State the blood parasite species.
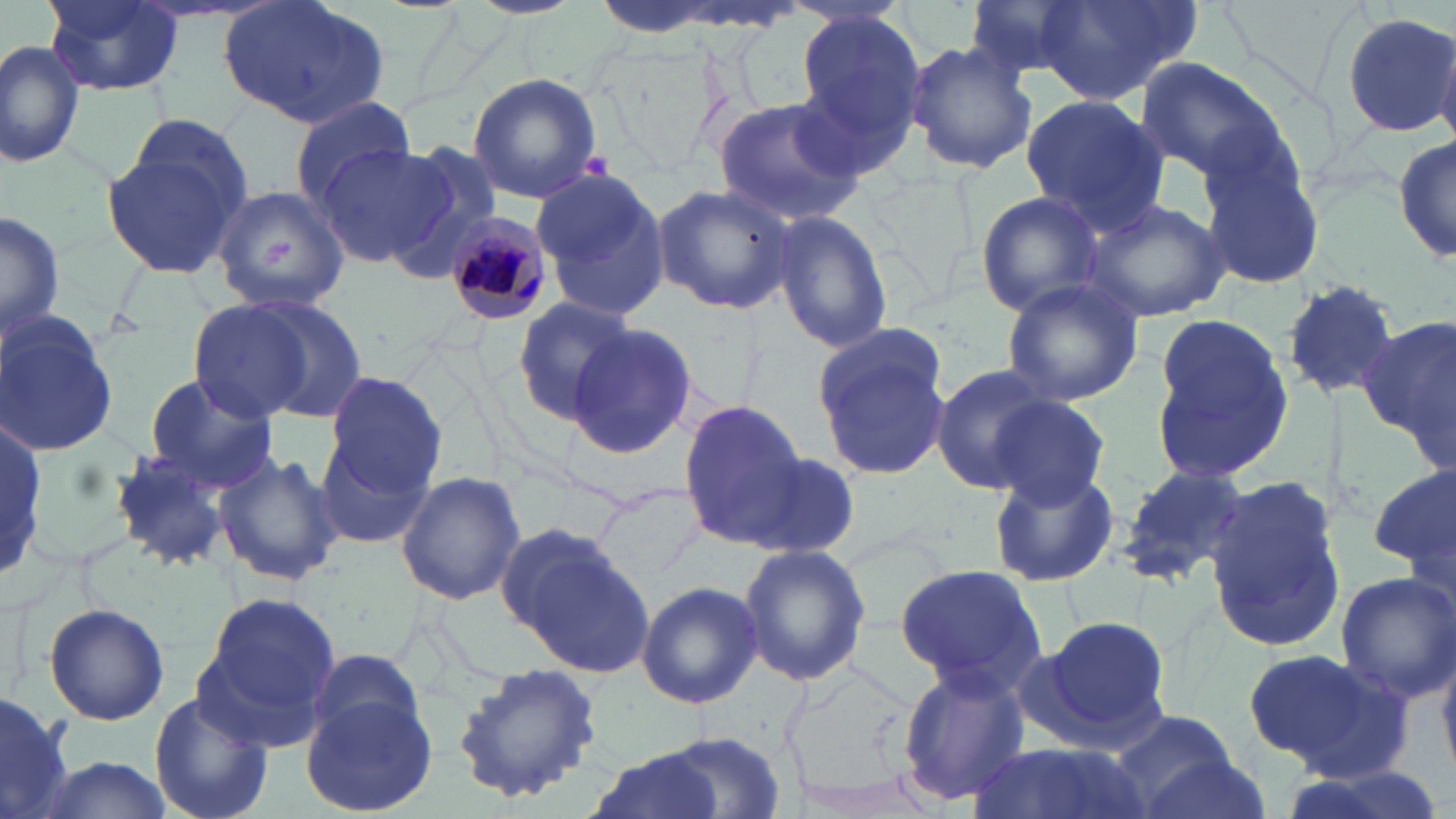

Plasmodium malariae.

modality: optical microscopy
image_size: 1456×819 pixels
field_of_view: single
preparation: thin blood film
stain: May-Grünwald-Giemsa
plasmodium_malariae_infected_red_blood_cell_locations: 'approximate bounding boxes as named x1/y1/x2/y2 corners in pixels: (x1=440, y1=215, x2=557, y2=327)'
uninfected_red_blood_cell_locations: 'approximate bounding boxes as named x1/y1/x2/y2 corners in pixels: (x1=42, y1=0, x2=185, y2=97), (x1=963, y1=0, x2=1089, y2=77), (x1=1035, y1=0, x2=1198, y2=105), (x1=221, y1=2, x2=391, y2=130), (x1=791, y1=9, x2=930, y2=169), (x1=1340, y1=10, x2=1456, y2=137), (x1=0, y1=37, x2=84, y2=170), (x1=905, y1=40, x2=1037, y2=174), (x1=1135, y1=58, x2=1290, y2=190), (x1=466, y1=72, x2=604, y2=205), (x1=712, y1=95, x2=867, y2=226), (x1=1019, y1=95, x2=1171, y2=232), (x1=289, y1=100, x2=419, y2=210), (x1=125, y1=115, x2=254, y2=225), (x1=1393, y1=128, x2=1455, y2=270), (x1=100, y1=137, x2=247, y2=282), (x1=314, y1=143, x2=454, y2=265), (x1=382, y1=143, x2=505, y2=274), (x1=1200, y1=155, x2=1329, y2=290), (x1=529, y1=169, x2=671, y2=320), (x1=653, y1=182, x2=796, y2=316), (x1=210, y1=184, x2=352, y2=315), (x1=973, y1=191, x2=1107, y2=317), (x1=1083, y1=198, x2=1227, y2=322), (x1=771, y1=209, x2=893, y2=356), (x1=1, y1=210, x2=65, y2=342), (x1=1001, y1=277, x2=1143, y2=406), (x1=1280, y1=279, x2=1403, y2=401), (x1=189, y1=293, x2=364, y2=427), (x1=510, y1=297, x2=637, y2=423), (x1=0, y1=308, x2=123, y2=456), (x1=1148, y1=314, x2=1295, y2=483), (x1=1360, y1=317, x2=1456, y2=458), (x1=566, y1=322, x2=704, y2=460), (x1=808, y1=325, x2=955, y2=480), (x1=927, y1=363, x2=1061, y2=494), (x1=324, y1=369, x2=448, y2=498), (x1=141, y1=371, x2=279, y2=494), (x1=986, y1=396, x2=1112, y2=512), (x1=678, y1=400, x2=807, y2=546), (x1=0, y1=406, x2=48, y2=592), (x1=316, y1=430, x2=436, y2=549), (x1=112, y1=446, x2=235, y2=573), (x1=750, y1=451, x2=863, y2=558), (x1=214, y1=452, x2=343, y2=588), (x1=987, y1=464, x2=1120, y2=587), (x1=1369, y1=464, x2=1455, y2=574), (x1=1115, y1=465, x2=1251, y2=586), (x1=395, y1=470, x2=526, y2=606), (x1=1204, y1=473, x2=1348, y2=657), (x1=591, y1=480, x2=706, y2=582), (x1=498, y1=524, x2=652, y2=675), (x1=737, y1=543, x2=871, y2=688), (x1=895, y1=564, x2=1047, y2=694), (x1=1333, y1=571, x2=1456, y2=702), (x1=636, y1=580, x2=763, y2=709), (x1=192, y1=589, x2=339, y2=747), (x1=42, y1=602, x2=170, y2=725), (x1=1030, y1=614, x2=1172, y2=754), (x1=305, y1=649, x2=427, y2=750), (x1=1242, y1=649, x2=1376, y2=761), (x1=448, y1=665, x2=607, y2=802), (x1=897, y1=665, x2=1029, y2=806), (x1=148, y1=689, x2=271, y2=819), (x1=0, y1=691, x2=74, y2=819), (x1=300, y1=692, x2=439, y2=817), (x1=1108, y1=709, x2=1245, y2=816), (x1=647, y1=732, x2=786, y2=815), (x1=966, y1=740, x2=1145, y2=819), (x1=581, y1=748, x2=728, y2=819), (x1=1132, y1=753, x2=1275, y2=819), (x1=23, y1=754, x2=174, y2=818)'
magnification: 1000x